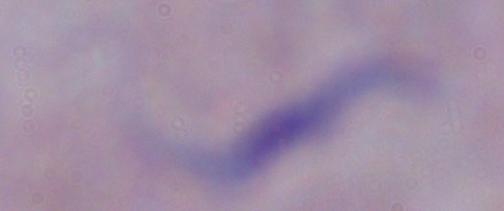 Photomicrograph. 1000x magnification. A trypanosome is shown.